Name the blood parasite species.
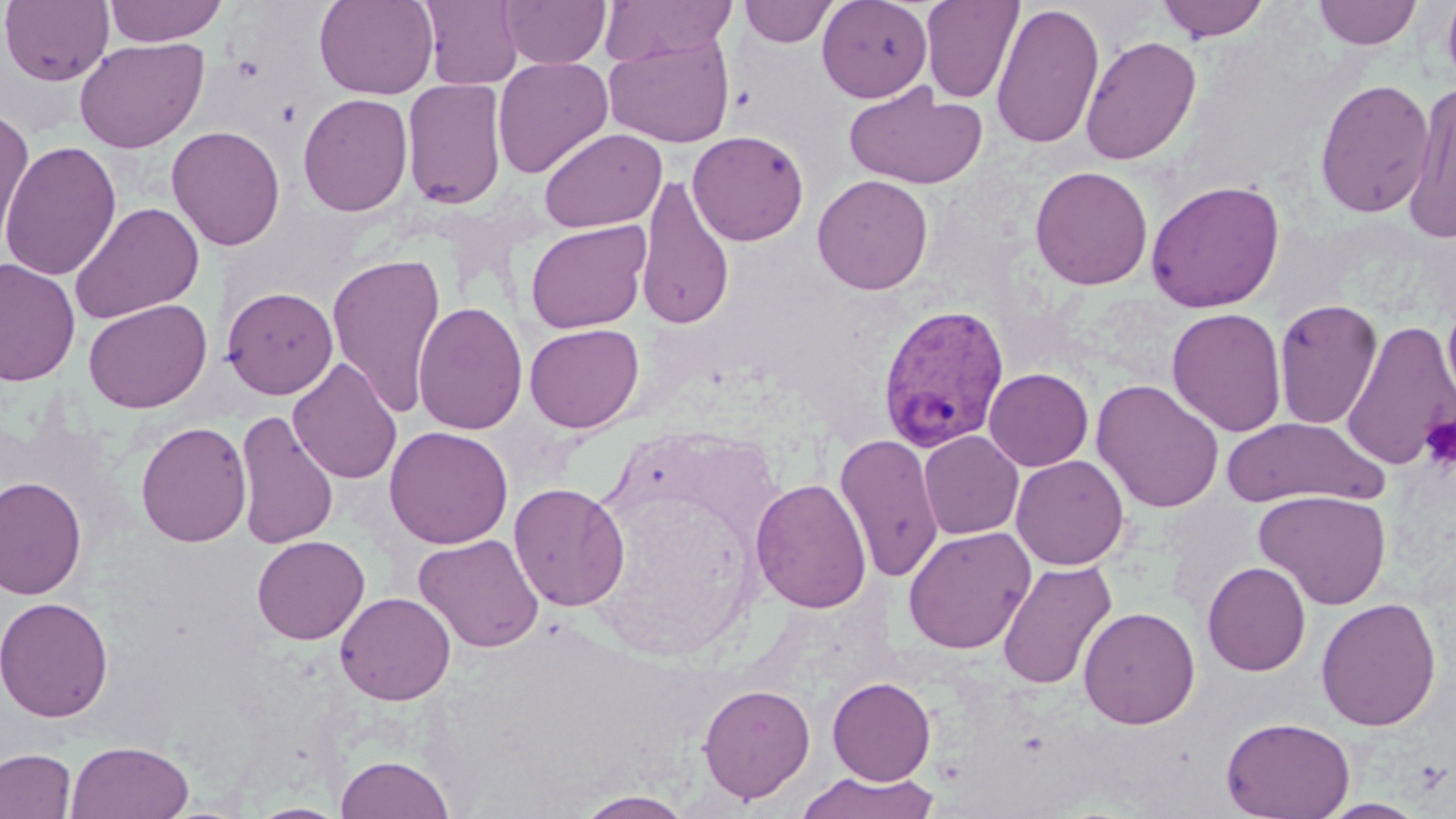

Plasmodium vivax.

Approximate bounding boxes as (x1, y1, x2, y2) in pixels. Plasmodium vivax-infected red blood cell locations: (877, 303, 1011, 453). Uninfected red blood cell locations: (1, 0, 114, 86), (104, 0, 227, 46), (313, 0, 439, 99), (419, 0, 523, 90), (500, 0, 611, 69), (599, 0, 738, 67), (817, 0, 933, 102), (921, 0, 1024, 104), (1156, 0, 1271, 42), (1314, 0, 1423, 49), (1442, 0, 1456, 95), (739, 1, 838, 47), (991, 3, 1105, 149), (604, 34, 735, 147), (1080, 35, 1201, 165), (73, 36, 210, 154), (492, 56, 613, 179), (401, 78, 508, 211), (1314, 78, 1435, 219), (1404, 82, 1456, 243), (843, 84, 988, 190), (298, 93, 413, 216), (0, 111, 35, 257), (166, 125, 286, 251), (538, 127, 666, 233), (687, 130, 809, 246), (0, 141, 122, 281), (1029, 166, 1154, 290), (812, 174, 933, 294), (635, 175, 735, 331), (1145, 179, 1285, 313), (70, 202, 205, 324), (525, 220, 651, 333), (327, 252, 447, 419), (0, 258, 80, 387), (222, 286, 339, 399), (1441, 294, 1456, 421), (83, 298, 213, 413), (1273, 298, 1383, 430), (412, 302, 528, 435), (1166, 307, 1287, 437), (1340, 319, 1455, 471), (524, 323, 645, 433), (288, 358, 402, 485), (984, 368, 1093, 471), (1091, 378, 1225, 513), (234, 409, 339, 549), (1222, 417, 1386, 508), (135, 420, 252, 547), (384, 425, 514, 549), (918, 430, 1024, 540), (834, 433, 945, 583), (1011, 455, 1129, 571), (0, 476, 87, 600), (751, 478, 872, 614), (508, 482, 630, 612), (1254, 489, 1392, 609), (902, 526, 1035, 655), (414, 534, 545, 653), (251, 535, 370, 645), (996, 560, 1118, 690), (1202, 561, 1311, 676), (335, 592, 456, 705), (0, 595, 114, 723), (1315, 596, 1442, 731), (1079, 606, 1200, 729), (827, 677, 936, 785), (698, 682, 816, 803), (1221, 716, 1355, 819), (65, 740, 194, 819), (0, 747, 77, 819), (335, 754, 454, 819), (797, 771, 940, 819), (574, 790, 695, 818), (1315, 799, 1431, 818), (248, 802, 349, 819). Platelet locations: (1420, 415, 1456, 473). Thin blood smear. May-Grünwald-Giemsa-stained preparation. Image is 1456×819 pixels. Single field of view. Optical microscopy. 1000x magnification.